Describe the morphology of the red blood cells.
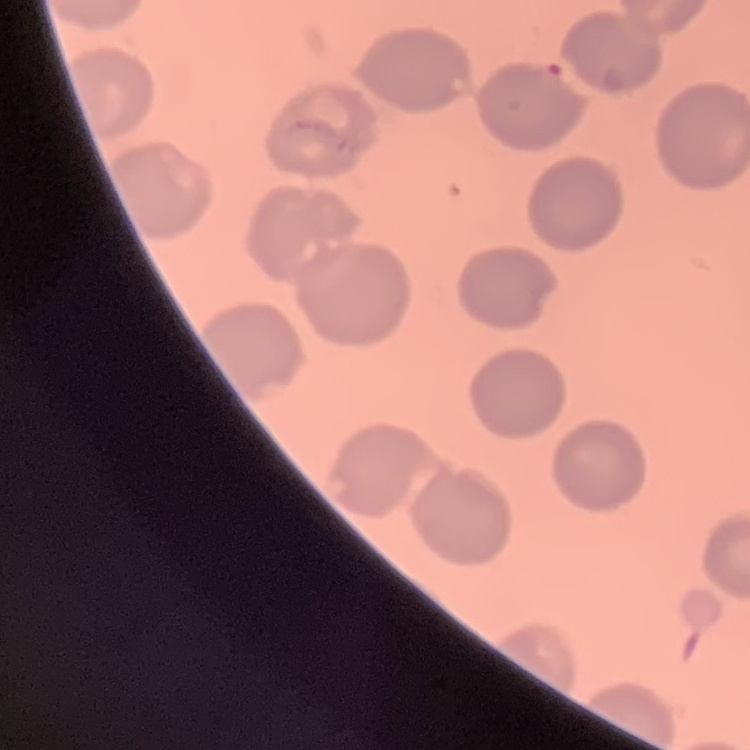

No rouleaux formation.

preparation = thin blood film
stain = Field's or Giemsa
image type = one tile cut from a larger photomicrograph